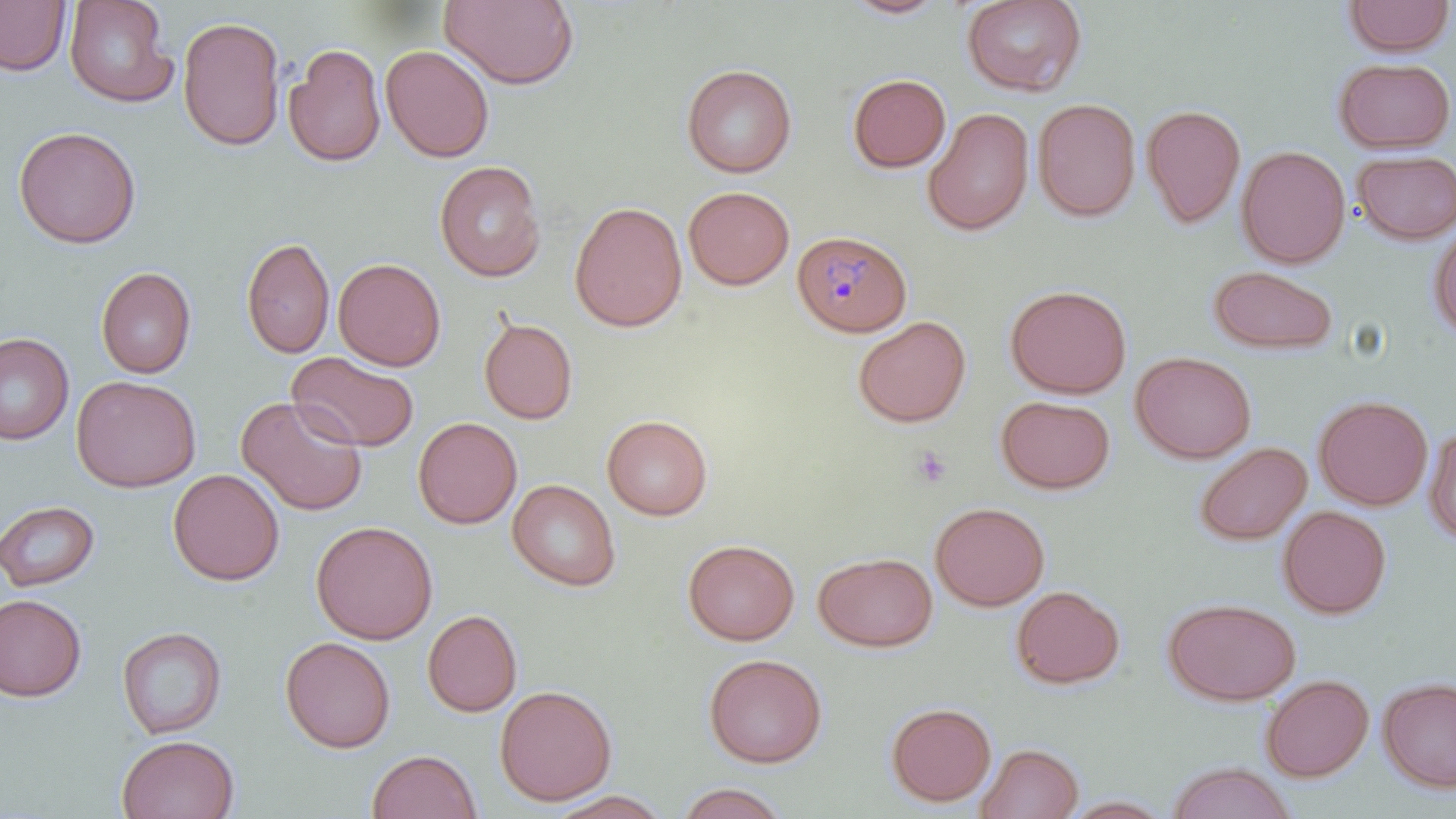

Summary:
  - Coordinate format: approximate bounding boxes as (x1, y1, x2, y2) in pixels
  - Uninfected red blood cell locations: (0, 0, 71, 76), (63, 0, 178, 108), (439, 0, 580, 89), (842, 0, 951, 20), (961, 0, 1088, 96), (1342, 0, 1454, 57), (177, 15, 286, 152), (283, 43, 387, 167), (381, 44, 494, 162), (1333, 57, 1455, 153), (681, 63, 797, 178), (847, 73, 951, 173), (1032, 97, 1141, 222), (1141, 103, 1246, 229), (922, 107, 1035, 236), (13, 126, 141, 248), (1236, 145, 1351, 268), (1352, 149, 1456, 244), (433, 160, 546, 282), (683, 186, 795, 290), (569, 200, 687, 332), (1428, 222, 1456, 342), (240, 236, 335, 359), (333, 258, 447, 371), (1208, 265, 1339, 355), (95, 267, 197, 379), (1005, 284, 1132, 399), (853, 315, 972, 428), (479, 316, 579, 425), (0, 333, 74, 445), (1130, 351, 1256, 463), (286, 352, 420, 452), (71, 375, 201, 492), (1313, 394, 1433, 510), (236, 395, 369, 516), (995, 395, 1116, 494), (602, 414, 713, 520), (412, 417, 522, 529), (1423, 424, 1456, 545), (1194, 441, 1312, 546), (168, 468, 285, 586), (507, 478, 621, 591), (0, 499, 100, 592), (930, 501, 1050, 611), (1278, 505, 1392, 618), (310, 520, 438, 644), (682, 539, 799, 645), (813, 552, 937, 652), (1011, 585, 1125, 689), (0, 594, 86, 702), (1163, 597, 1301, 706), (422, 609, 522, 717), (116, 625, 228, 740), (280, 636, 396, 753), (704, 652, 828, 768), (1260, 674, 1374, 782), (1377, 676, 1456, 793), (494, 684, 617, 806), (885, 702, 997, 807), (116, 734, 240, 819), (975, 742, 1084, 819), (367, 749, 481, 819), (1165, 762, 1298, 819), (674, 782, 791, 818), (546, 790, 674, 818), (1060, 795, 1176, 818)
  - Plasmodium malariae-infected red blood cell locations: (792, 229, 912, 338)
  - Slide-level diagnosis: Plasmodium malariae
  - Preparation: thin blood film
  - Field of view: one of a larger specimen
  - Modality: optical microscopy
  - Magnification: 1000x
  - Image size: 1456×819 pixels
  - Stain: May-Grünwald-Giemsa